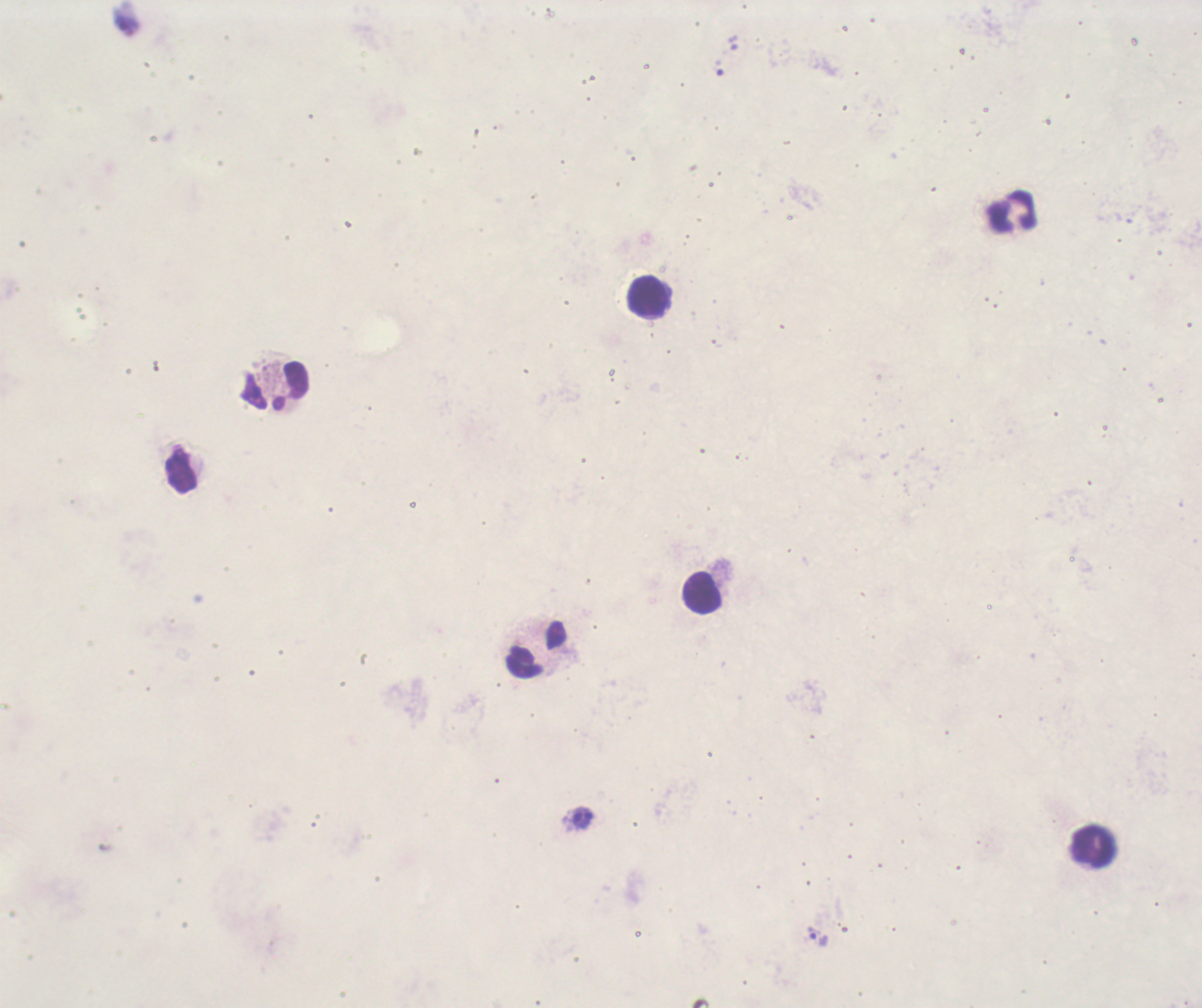

Approximate centers as {x, y} in pixels.
Summary:
  - Leukocyte locations: {1012, 211}, {648, 298}, {274, 389}, {181, 471}, {703, 595}, {536, 649}, {1093, 847}
  - Trophozoite locations: {125, 22}, {733, 42}, {816, 936}
  - Context: previously used in an actual diagnosis
  - Image size: 1202×1008 pixels
  - Coloration quality: bad
  - Field of view: single
  - Result: positive for Plasmodium parasites
  - Magnification: 100x
  - Background quality: poor
  - Stain: Romanowsky
  - Preparation: thick blood smear